Comment on the morphology of the erythrocytes.
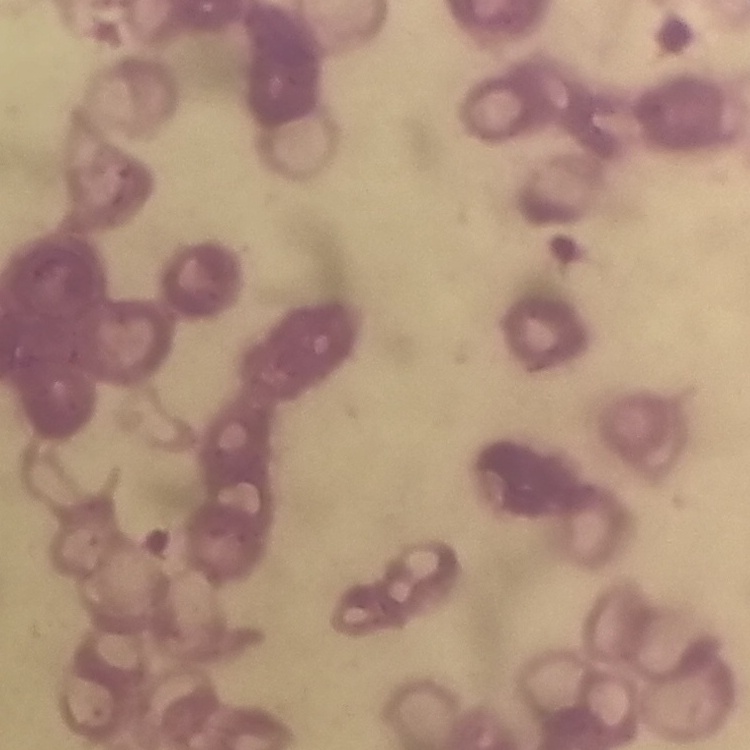
Rouleaux formation.

{
  "preparation": "thin peripheral smear",
  "image_type": "square crop of a larger photomicrograph",
  "stain": "Field's or Giemsa"
}